State which parasite is depicted.
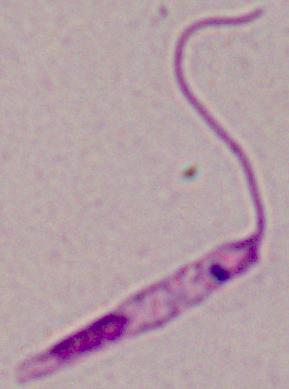
This is Leishmania.

Summary:
  - Modality: micrograph
  - Magnification: 1000x